Report the malaria status of this cell.
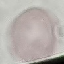

It is uninfected.

preparation = thin blood smear
stain = Giemsa
capture = smartphone camera at the microscope eyepiece
image type = automatically extracted cell patch, resized to 64 × 64 pixels